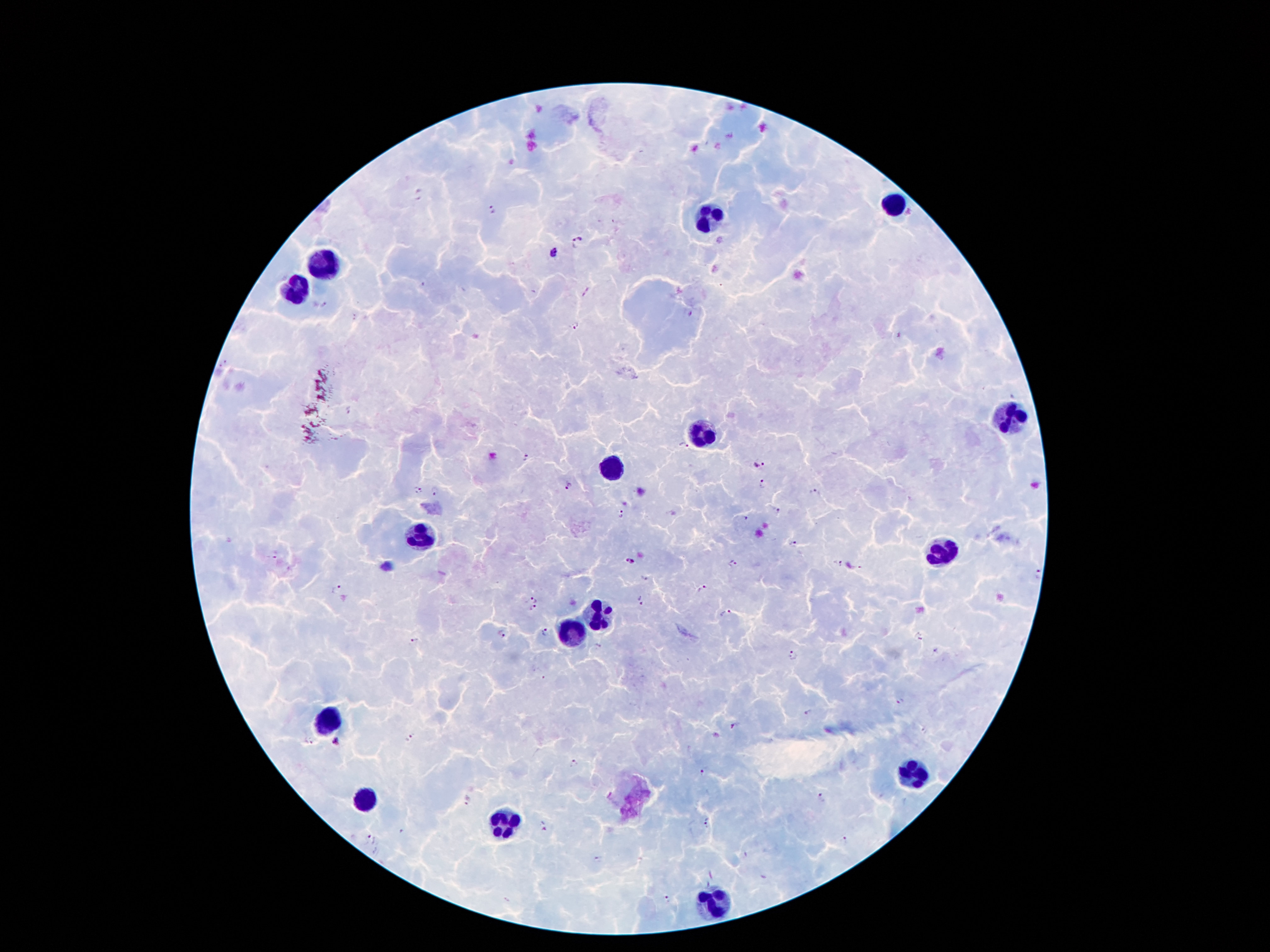
Approximate centers as {x, y} in pixels. Malaria parasite locations: {491, 211}, {578, 244}, {554, 252}, {577, 326}, {348, 411}, {683, 446}, {527, 457}, {756, 462}, {761, 484}, {567, 486}, {418, 490}, {439, 491}, {816, 494}, {775, 510}, {622, 517}, {747, 518}, {792, 542}, {275, 555}, {629, 560}, {733, 562}, {838, 564}, {1039, 574}, {644, 577}, {336, 591}, {703, 591}, {532, 599}, {639, 600}, {534, 609}, {724, 614}, {545, 630}, {502, 633}, {919, 637}, {415, 639}, {936, 651}, {795, 656}, {900, 701}, {807, 711}, {735, 725}, {410, 739}, {337, 741}, {573, 764}, {704, 772}, {820, 797}, {466, 799}, {706, 824}, {543, 829}, {368, 839}, {845, 841}, {598, 860}, {667, 898}. Leukocyte locations: {895, 205}, {709, 219}, {327, 261}, {295, 293}, {1009, 417}, {701, 435}, {611, 469}, {421, 539}, {937, 555}, {595, 617}, {573, 629}, {327, 719}, {917, 773}, {365, 803}, {499, 824}, {713, 902}. Smartphone photograph taken through the microscope eyepiece. Patient malaria status: infected with Plasmodium falciparum. Thick peripheral-blood smear. 100x magnification. Single field of view. Giemsa-stained preparation. Image is 1270×952 pixels.